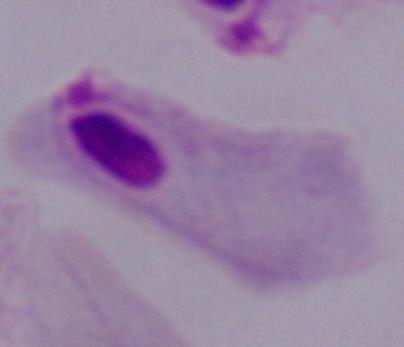

Photomicrograph. A trichomonad is seen. 1000x magnification.